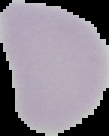

Summary:
  - Malaria status: uninfected
  - Image type: cell region segmented out of the field of view; surrounding area masked to black
  - Preparation: thin blood smear
  - Image size: 109×136 pixels